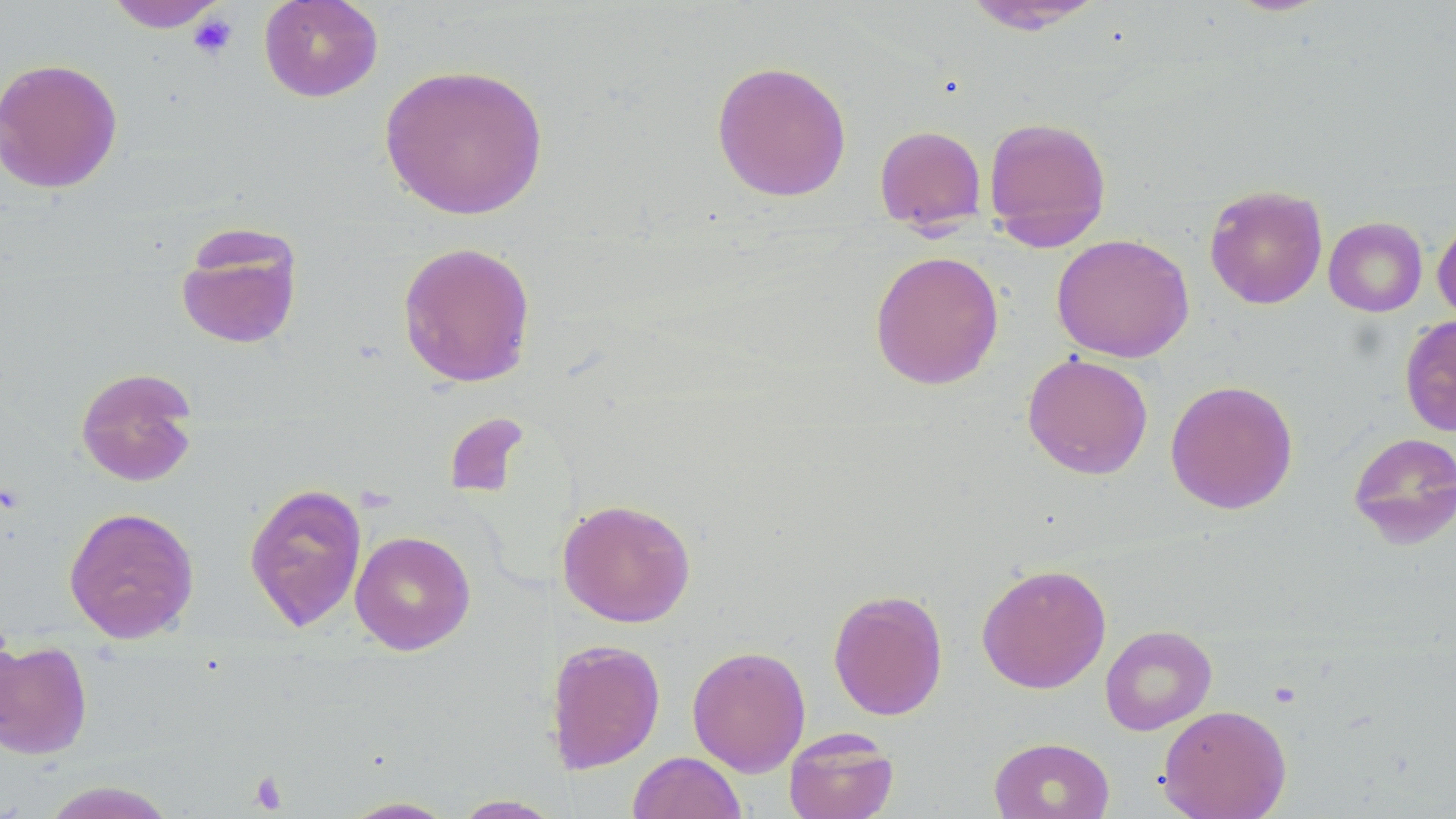

slide-level diagnosis = negative for blood parasites
magnification = 1000x
stain = May-Grünwald-Giemsa
modality = optical microscopy
uninfected red blood cell locations = approximate bounding boxes as (x1, y1, x2, y2) in pixels: (258, 0, 384, 102), (103, 1, 229, 32), (959, 1, 1109, 33), (0, 57, 124, 195), (711, 60, 852, 202), (378, 62, 550, 221), (982, 115, 1113, 249), (874, 124, 987, 230), (1204, 184, 1328, 309), (1432, 214, 1456, 322), (1323, 217, 1427, 317), (173, 224, 304, 351), (1051, 233, 1195, 363), (397, 241, 536, 388), (869, 249, 1004, 390), (1399, 314, 1456, 437), (1022, 352, 1154, 479), (74, 366, 200, 488), (1165, 379, 1299, 515), (443, 411, 531, 501), (1347, 431, 1456, 548), (243, 481, 368, 632), (557, 498, 697, 627), (63, 506, 200, 643), (350, 530, 476, 655), (976, 562, 1112, 694), (827, 588, 949, 721), (1100, 625, 1217, 736), (0, 638, 93, 760), (555, 638, 666, 774), (687, 644, 811, 776), (1158, 704, 1292, 818), (783, 728, 900, 819), (989, 736, 1115, 819), (628, 751, 747, 819), (38, 780, 181, 819), (450, 795, 564, 818), (337, 796, 460, 818)
preparation = thin blood film
image size = 1456×819 pixels
field of view = single
platelet locations = approximate bounding boxes as (x1, y1, x2, y2) in pixels: (189, 10, 239, 61), (248, 771, 288, 813)